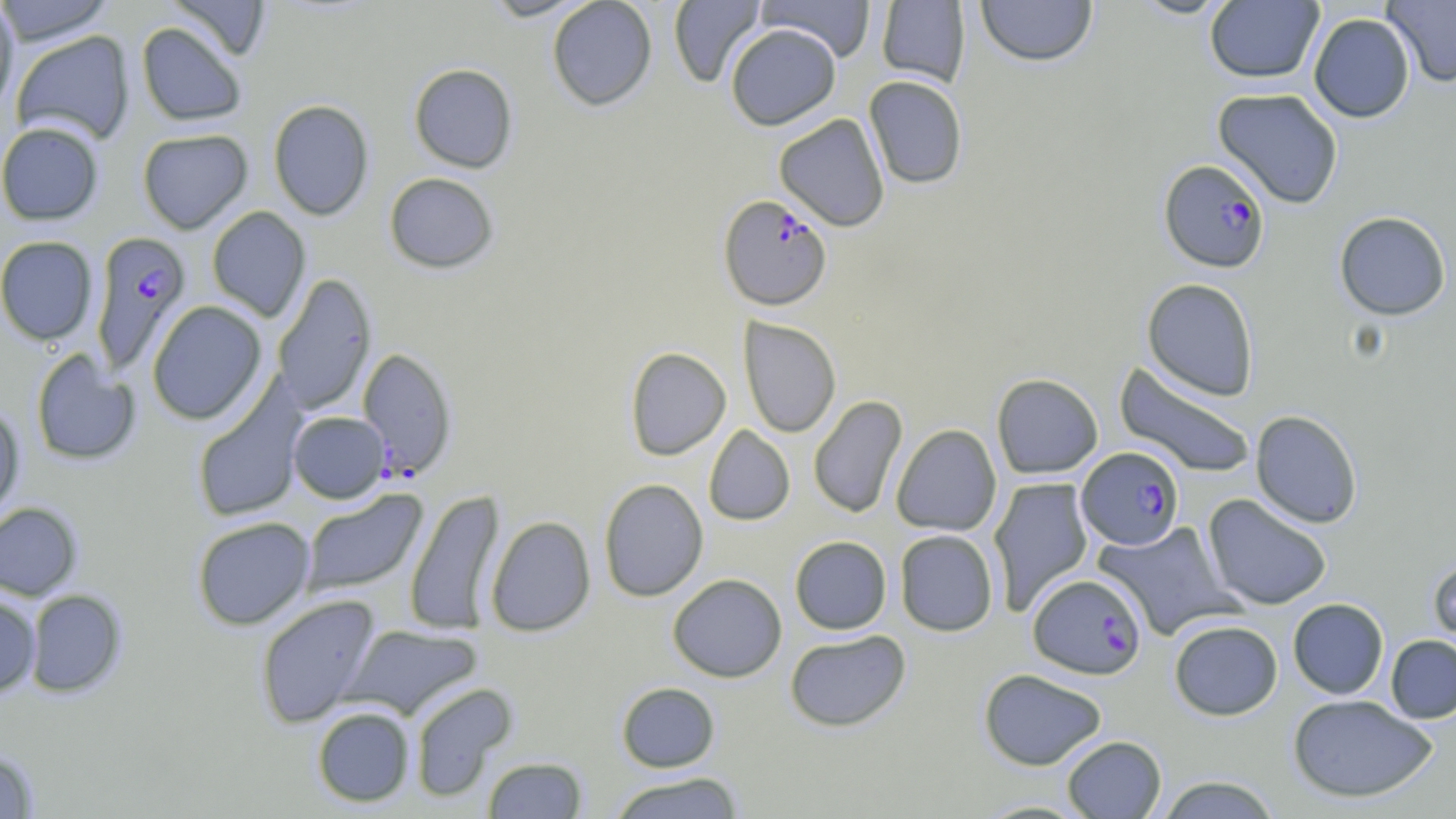

slide_level_diagnosis: Plasmodium falciparum
image_size: 1456×819 pixels
magnification: 1000x
field_of_view: one of a larger specimen
modality: optical microscopy
uninfected_red_blood_cell_locations: 'approximate bounding boxes as (x1,y1)-(x2,y2) corner pairs in pixels: (0,0)-(115,45), (166,0)-(272,61), (481,0)-(593,21), (547,0)-(657,111), (668,0)-(766,88), (757,0)-(876,62), (975,0)-(1097,67), (1129,0)-(1237,19), (1383,0)-(1456,87), (0,1)-(19,116), (876,1)-(971,88), (1205,1)-(1324,84), (1308,13)-(1415,123), (136,22)-(247,126), (724,23)-(841,130), (11,31)-(135,144), (408,63)-(519,173), (863,75)-(968,189), (1212,88)-(1344,208), (268,99)-(375,221), (774,113)-(890,232), (0,122)-(104,225), (137,129)-(253,233), (384,172)-(499,274), (206,206)-(311,322), (1334,211)-(1451,321), (0,236)-(99,345), (272,273)-(377,414), (1142,278)-(1260,401), (147,301)-(268,425), (738,317)-(841,438), (624,346)-(731,460), (31,350)-(141,466), (1114,362)-(1257,479), (991,373)-(1103,479), (192,382)-(306,522), (808,395)-(908,519), (0,406)-(25,523), (1250,409)-(1363,528), (288,411)-(390,503), (890,424)-(1002,536), (703,425)-(795,526), (988,477)-(1094,614), (598,478)-(709,602), (300,489)-(428,597), (404,489)-(505,637), (1202,494)-(1333,611), (0,502)-(83,601), (191,516)-(316,630), (485,516)-(596,637), (1094,522)-(1236,639), (894,529)-(998,636), (789,535)-(892,635), (1427,554)-(1456,663), (667,573)-(787,682), (24,589)-(128,698), (254,593)-(382,729), (0,594)-(41,698), (1288,598)-(1389,699), (1169,619)-(1283,720), (340,624)-(483,719), (785,630)-(911,732), (1385,634)-(1456,724), (978,668)-(1108,770), (616,681)-(720,772), (408,682)-(517,801), (1288,694)-(1438,803), (312,706)-(416,807), (1061,735)-(1167,818), (0,750)-(40,818), (482,756)-(588,818), (607,772)-(745,818), (1154,774)-(1282,818), (972,799)-(1094,818)'
stain: May-Grünwald-Giemsa
plasmodium_falciparum_infected_red_blood_cell_locations: 'approximate bounding boxes as (x1,y1)-(x2,y2) corner pairs in pixels: (1159,158)-(1271,273), (717,195)-(833,312), (90,230)-(193,374), (357,347)-(458,480), (1077,446)-(1184,550), (1027,573)-(1147,679)'
preparation: thin blood film